Report the malaria status of this cell.
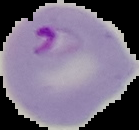
Parasitized.

Segmented cell region on a black background. From a thin blood film. Image is 139×130 pixels.